Classify this cell by malaria status.
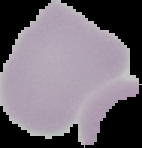
Uninfected.

{
  "image_size": "142×148 pixels",
  "image_type": "cell region segmented out of the field of view; surrounding area masked to black",
  "preparation": "thin blood smear"
}